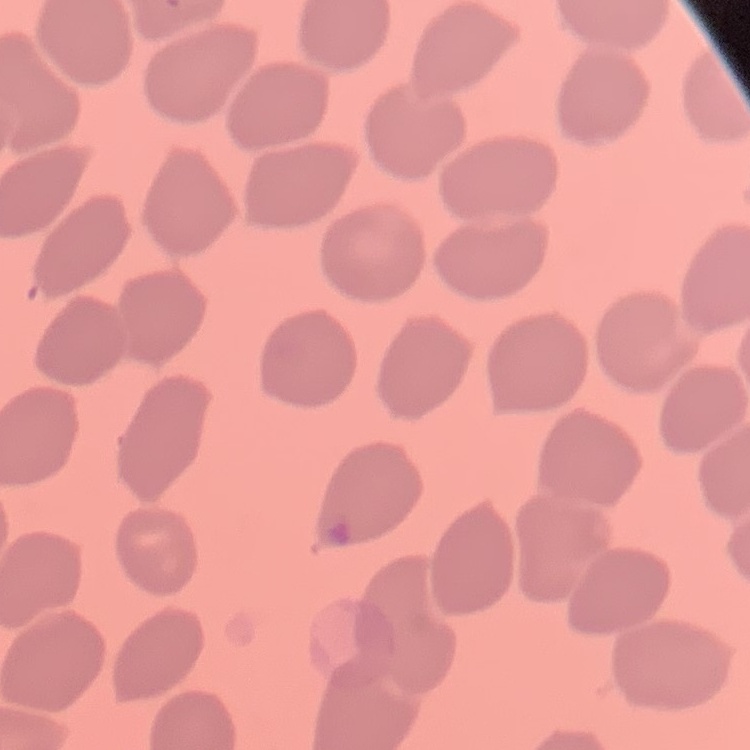

erythrocyte morphology = no rouleaux formation
stain = Field's or Giemsa
image type = one tile cut from a larger photomicrograph
preparation = thin peripheral smear